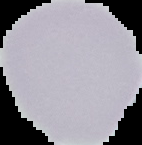 From a thin blood film. Image is 142×145 pixels. Malaria status: uninfected. The area outside the segmented cell region is set to black.